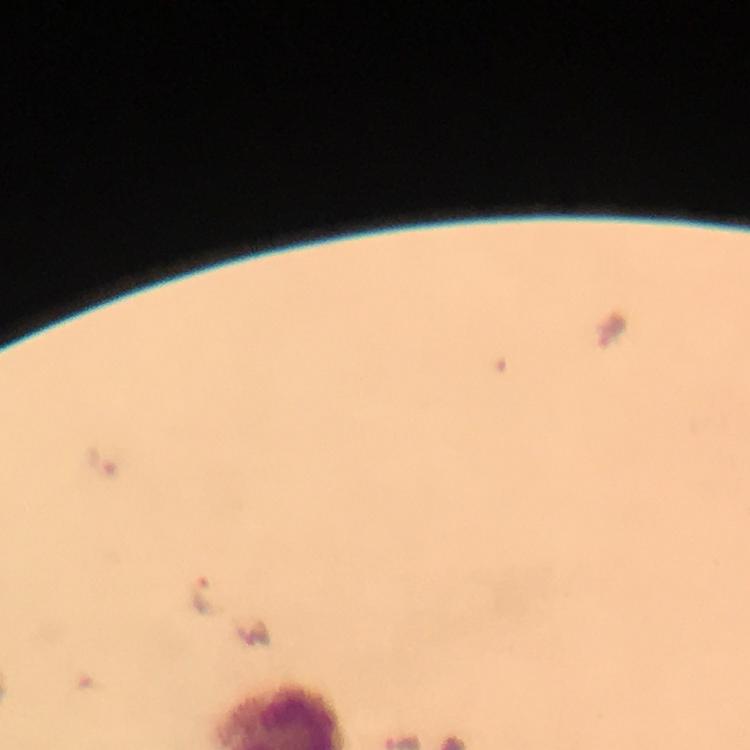

{
  "immersion_oil": "applied",
  "magnification": "100x",
  "cropped_from": "one field of view",
  "plasmodium_parasite_locations": "approximate centers as {x, y} in pixels: {103, 459}, {206, 596}",
  "capture": "smartphone photograph through a microscope",
  "preparation": "thick blood smear",
  "image_size": "750×750 pixels",
  "stain": "Giemsa",
  "context": "from a diagnostic examination for malaria"
}